Give the position of every leukocyte visible.
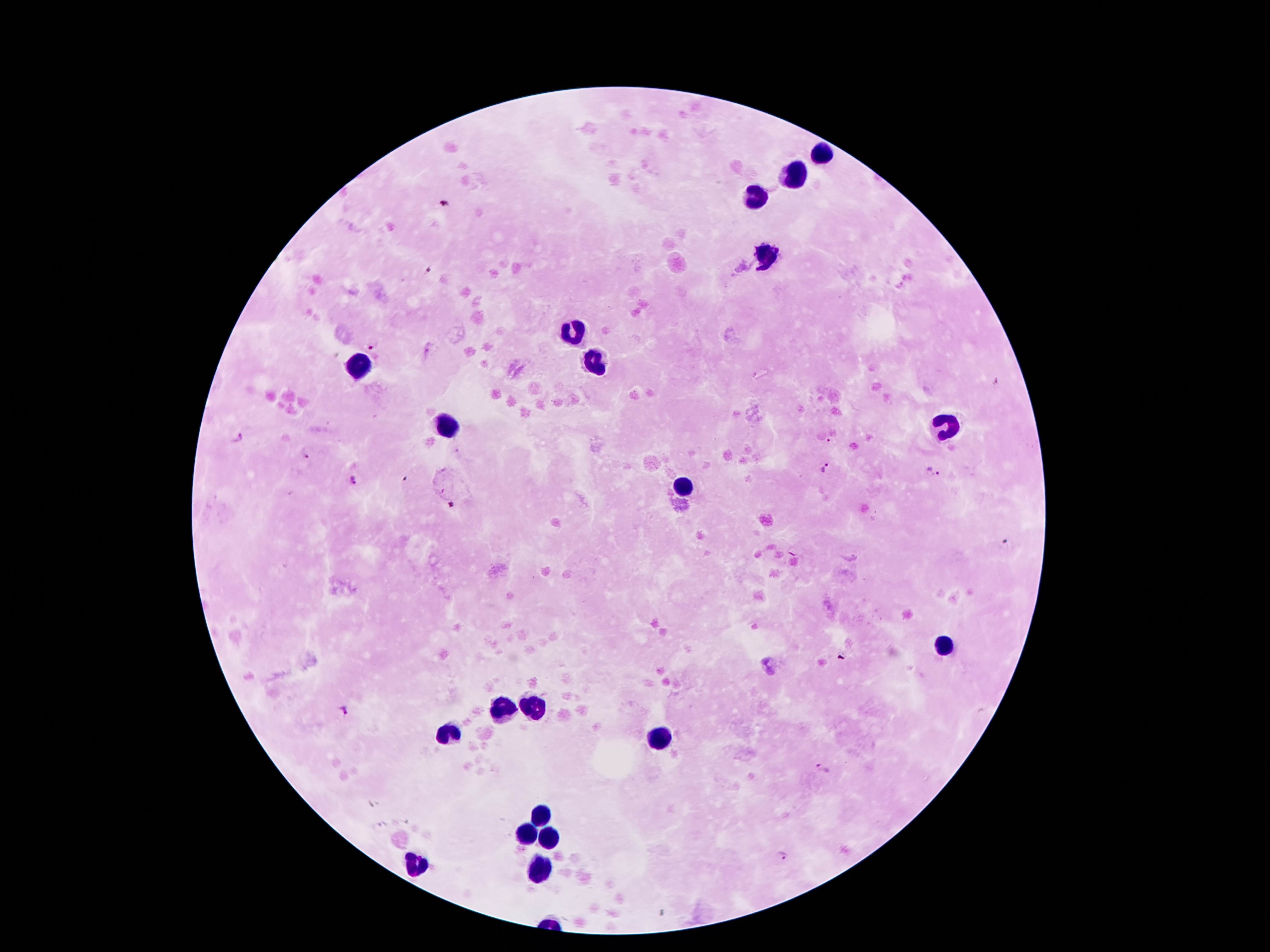
Approximate centers as (x, y) in pixels.
Leukocytes: (820, 154), (792, 177), (757, 196), (767, 255), (575, 331), (589, 364), (361, 367), (447, 429), (947, 429), (683, 486), (944, 645), (501, 710), (534, 710), (447, 736), (657, 736), (543, 815), (524, 833), (548, 841), (414, 864), (541, 868).

Summary:
  - Malaria parasite locations: (374, 343), (996, 381), (236, 437), (306, 454), (825, 468), (933, 473), (355, 480), (343, 712), (823, 770), (782, 857)
  - Magnification: 100x
  - Capture: smartphone camera through the microscope eyepiece
  - Stain: Giemsa
  - Image size: 1270×952 pixels
  - Preparation: thick peripheral-blood smear
  - Patient malaria status: infected with Plasmodium falciparum
  - Field of view: single